Identify the parasite.
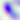

This is Toxoplasma gondii.

Photomicrograph. Captured at 400x magnification.